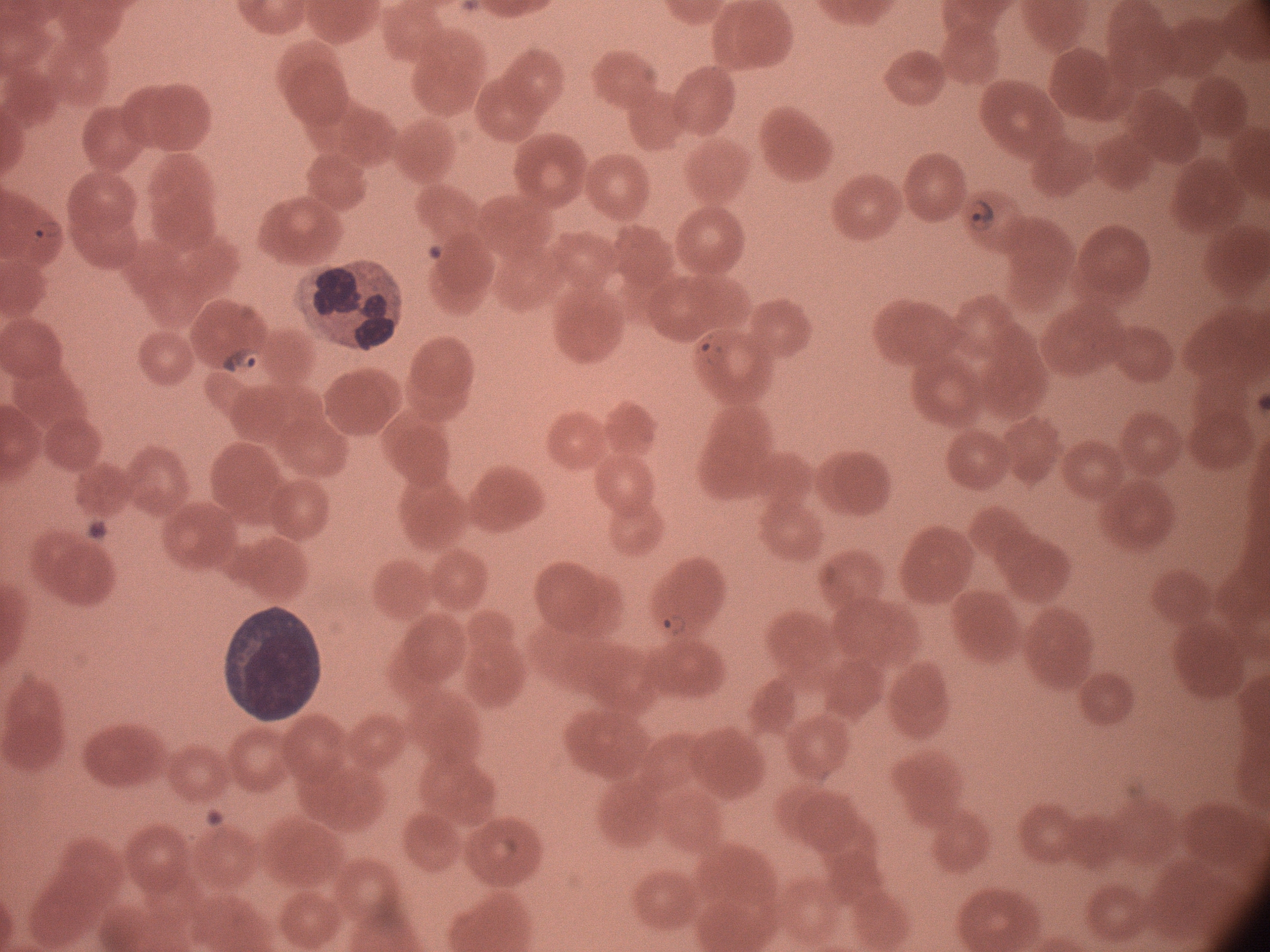

field_of_view: single
stain: Giemsa
image_size: 1270×952 pixels
microscope: Leica DM2000 with built-in camera
preparation: thin blood smear
magnification: 100x
ring_form_locations: 'approximate bounding boxes as [x1, y1, x2, y2] in pixels, from the source annotation, which is not necessarily exhaustive: [963, 190, 1001, 241], [24, 213, 71, 247], [683, 324, 728, 370], [212, 343, 272, 382], [657, 607, 697, 645]'
species: Plasmodium falciparum